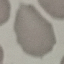

malaria status = uninfected
preparation = thin blood film
image type = cell patch, automatically extracted from a larger field of view and resized to 64 × 64 pixels
stain = Giemsa
capture = smartphone through the microscope eyepiece